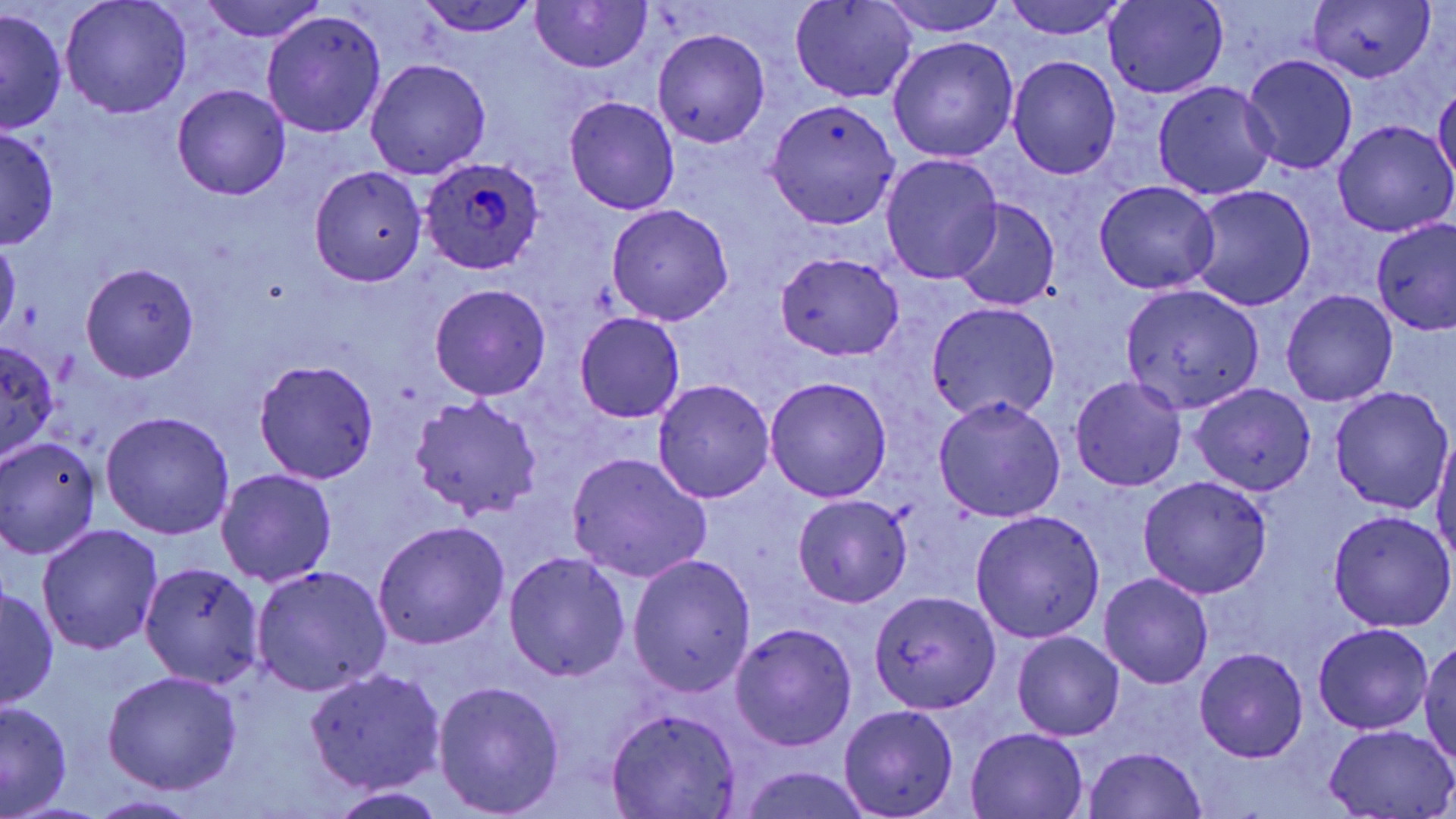
slide-level diagnosis = Plasmodium ovale
stain = May-Grünwald-Giemsa
modality = light microscopy
Plasmodium ovale-infected red blood cell locations = approximate bounding boxes as named x1/y1/x2/y2 corners in pixels: (x1=419, y1=159, x2=544, y2=275)
uninfected red blood cell locations = approximate bounding boxes as named x1/y1/x2/y2 corners in pixels: (x1=60, y1=0, x2=192, y2=119), (x1=412, y1=0, x2=542, y2=36), (x1=530, y1=0, x2=651, y2=75), (x1=875, y1=0, x2=1013, y2=36), (x1=1000, y1=0, x2=1127, y2=40), (x1=1103, y1=0, x2=1227, y2=99), (x1=1309, y1=0, x2=1433, y2=82), (x1=197, y1=1, x2=329, y2=42), (x1=790, y1=1, x2=919, y2=104), (x1=262, y1=10, x2=386, y2=137), (x1=1, y1=11, x2=67, y2=134), (x1=652, y1=28, x2=770, y2=146), (x1=887, y1=36, x2=1020, y2=162), (x1=1241, y1=54, x2=1358, y2=177), (x1=1008, y1=56, x2=1121, y2=180), (x1=365, y1=58, x2=492, y2=179), (x1=1152, y1=80, x2=1278, y2=201), (x1=1433, y1=81, x2=1456, y2=186), (x1=171, y1=84, x2=291, y2=200), (x1=563, y1=95, x2=680, y2=214), (x1=765, y1=98, x2=900, y2=228), (x1=1332, y1=120, x2=1455, y2=237), (x1=0, y1=129, x2=60, y2=248), (x1=880, y1=153, x2=1003, y2=284), (x1=308, y1=164, x2=428, y2=287), (x1=1093, y1=179, x2=1221, y2=294), (x1=1188, y1=185, x2=1316, y2=311), (x1=948, y1=200, x2=1060, y2=311), (x1=605, y1=204, x2=733, y2=324), (x1=1372, y1=217, x2=1456, y2=337), (x1=0, y1=237, x2=21, y2=340), (x1=777, y1=254, x2=905, y2=359), (x1=81, y1=263, x2=199, y2=382), (x1=430, y1=285, x2=550, y2=400), (x1=1121, y1=285, x2=1265, y2=413), (x1=1282, y1=289, x2=1397, y2=407), (x1=924, y1=301, x2=1060, y2=421), (x1=574, y1=312, x2=685, y2=424), (x1=0, y1=343, x2=61, y2=461), (x1=253, y1=356, x2=381, y2=485), (x1=764, y1=375, x2=893, y2=502), (x1=1071, y1=376, x2=1187, y2=492), (x1=652, y1=378, x2=775, y2=503), (x1=1189, y1=382, x2=1317, y2=496), (x1=1328, y1=386, x2=1452, y2=515), (x1=935, y1=394, x2=1065, y2=521), (x1=409, y1=396, x2=543, y2=520), (x1=100, y1=411, x2=236, y2=539), (x1=1431, y1=433, x2=1456, y2=562), (x1=0, y1=437, x2=99, y2=557), (x1=565, y1=452, x2=712, y2=582), (x1=217, y1=468, x2=338, y2=588), (x1=1138, y1=476, x2=1271, y2=599), (x1=792, y1=495, x2=913, y2=607), (x1=970, y1=509, x2=1105, y2=643), (x1=1328, y1=510, x2=1456, y2=630), (x1=372, y1=521, x2=509, y2=650), (x1=35, y1=524, x2=164, y2=656), (x1=504, y1=552, x2=630, y2=682), (x1=630, y1=555, x2=756, y2=697), (x1=139, y1=561, x2=265, y2=689), (x1=250, y1=565, x2=391, y2=697), (x1=1099, y1=573, x2=1214, y2=689), (x1=2, y1=583, x2=58, y2=711), (x1=868, y1=590, x2=1001, y2=714), (x1=730, y1=623, x2=857, y2=751), (x1=1313, y1=623, x2=1434, y2=734), (x1=1012, y1=632, x2=1124, y2=741), (x1=1419, y1=638, x2=1456, y2=764), (x1=1193, y1=647, x2=1307, y2=762), (x1=302, y1=667, x2=446, y2=794), (x1=102, y1=671, x2=243, y2=794), (x1=433, y1=680, x2=565, y2=816), (x1=0, y1=702, x2=72, y2=816), (x1=839, y1=704, x2=959, y2=818), (x1=605, y1=706, x2=742, y2=818), (x1=1323, y1=723, x2=1456, y2=817), (x1=966, y1=727, x2=1088, y2=818), (x1=1082, y1=746, x2=1208, y2=819), (x1=736, y1=767, x2=875, y2=819), (x1=327, y1=788, x2=452, y2=816), (x1=85, y1=796, x2=203, y2=819)
preparation = thin blood smear
magnification = 1000x
field of view = single
image size = 1456×819 pixels